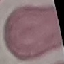

Summary:
  - Malaria status: uninfected
  - Capture: smartphone camera at the microscope eyepiece
  - Stain: Giemsa
  - Image type: cell patch, automatically extracted from a larger field of view and resized to 64 × 64 pixels
  - Preparation: thin smear